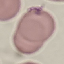
Summary:
  - Result: no malaria parasites seen
  - Stain: Giemsa
  - Preparation: thin smear
  - Image type: cell patch, automatically extracted from a larger field of view and resized to 64 × 64 pixels
  - Capture: smartphone through the microscope eyepiece